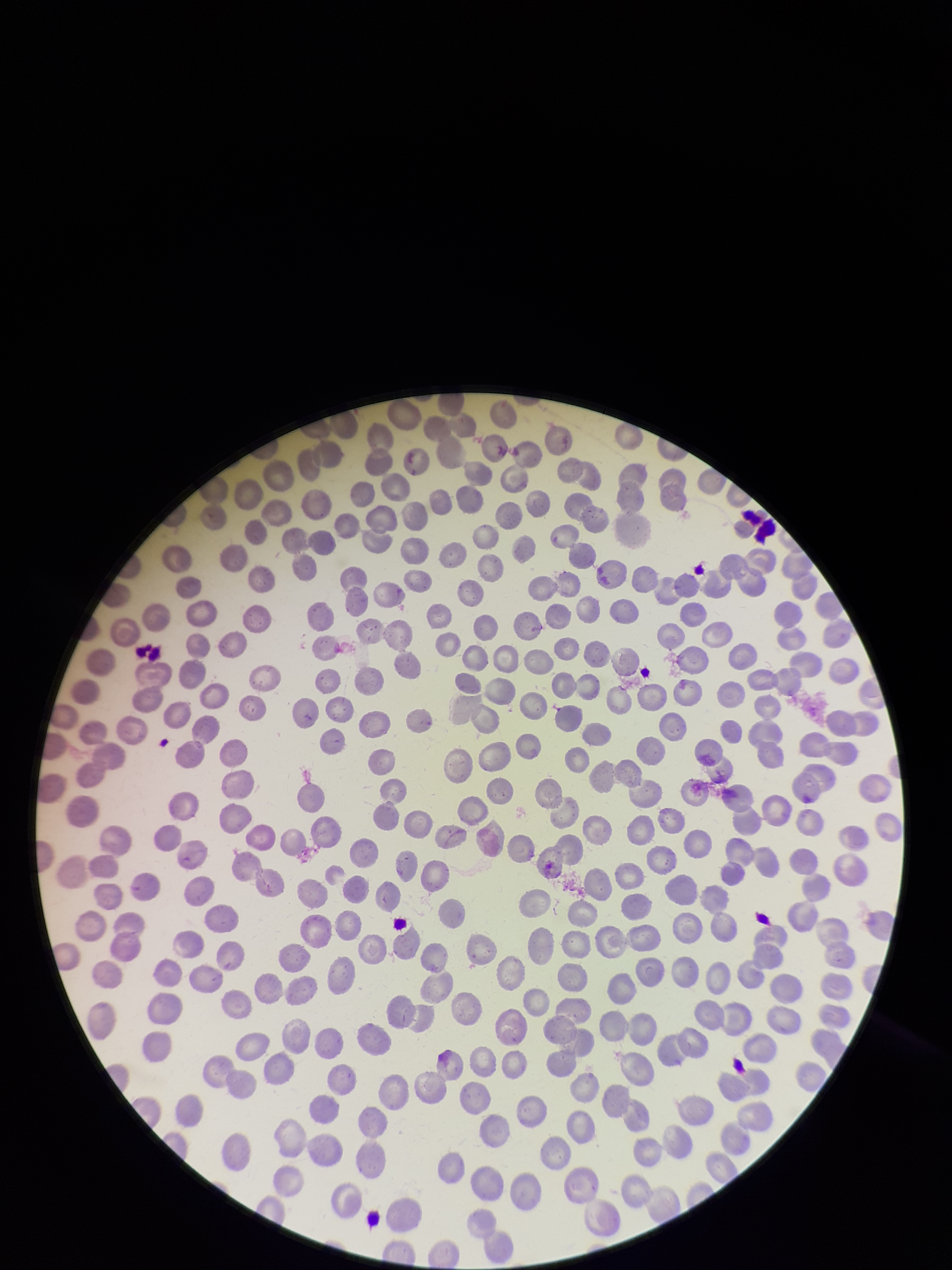
red blood cell count = 339
image size = 952×1270 pixels
stain = Giemsa
capture = smartphone photograph through the microscope eyepiece
parasitized red blood cell count = 0
parasitized red blood cells = none seen
patient malaria status = negative
field of view = single
preparation = thin blood smear